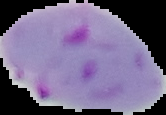
preparation = thin blood smear
result = malaria parasites detected
image size = 166×115 pixels
image type = segmented cell region on a black background